State the preparation type.
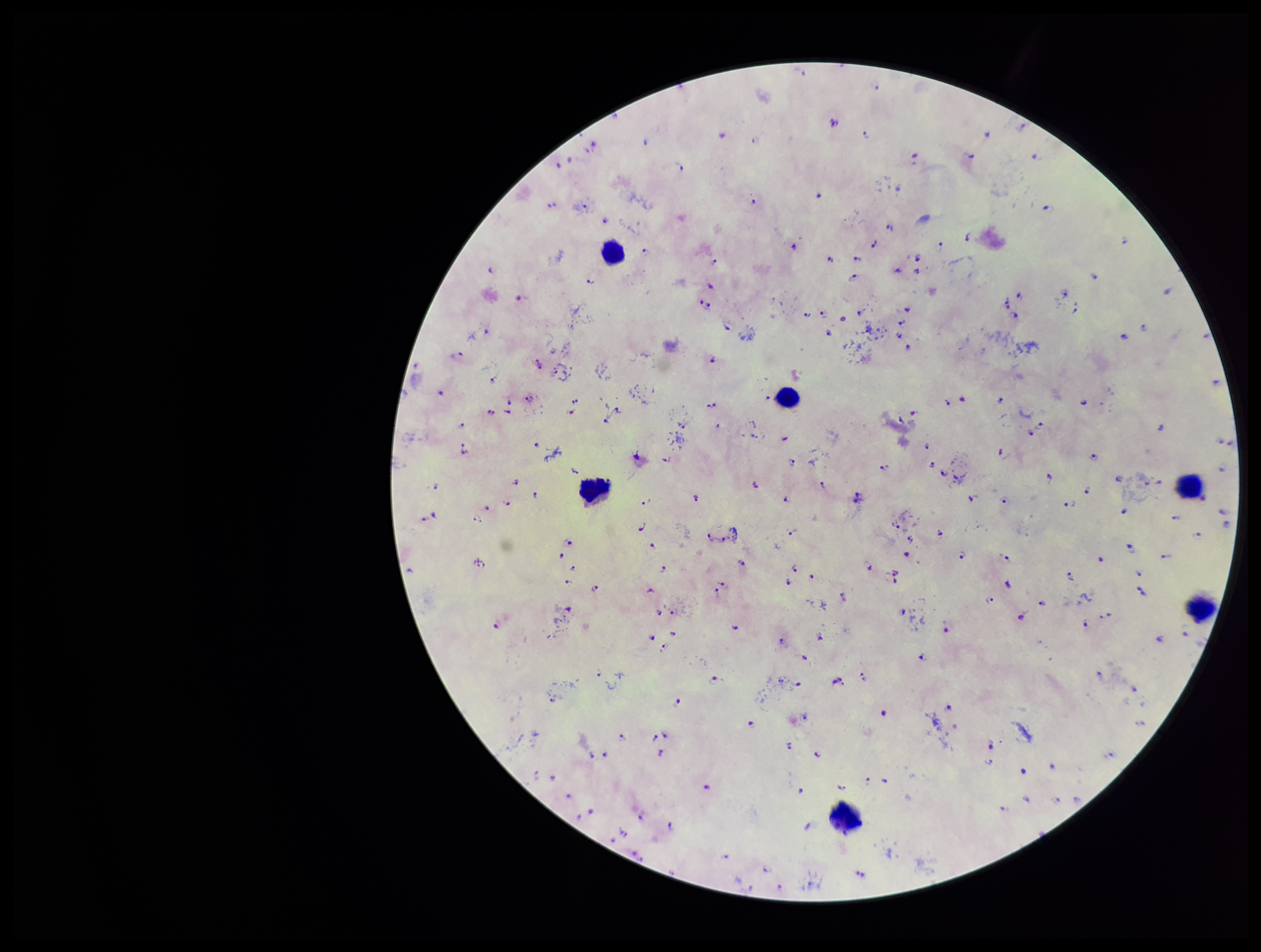

It is a thick blood smear.

stain = Giemsa
leukocyte count = 6
field of view = one from this slide
species reported for this patient = Plasmodium falciparum
parasite count = 175
image size = 1261×952 pixels
patient malaria status = infected
Plasmodium parasites = identified
capture = smartphone photograph through the microscope eyepiece